State the blood parasite species.
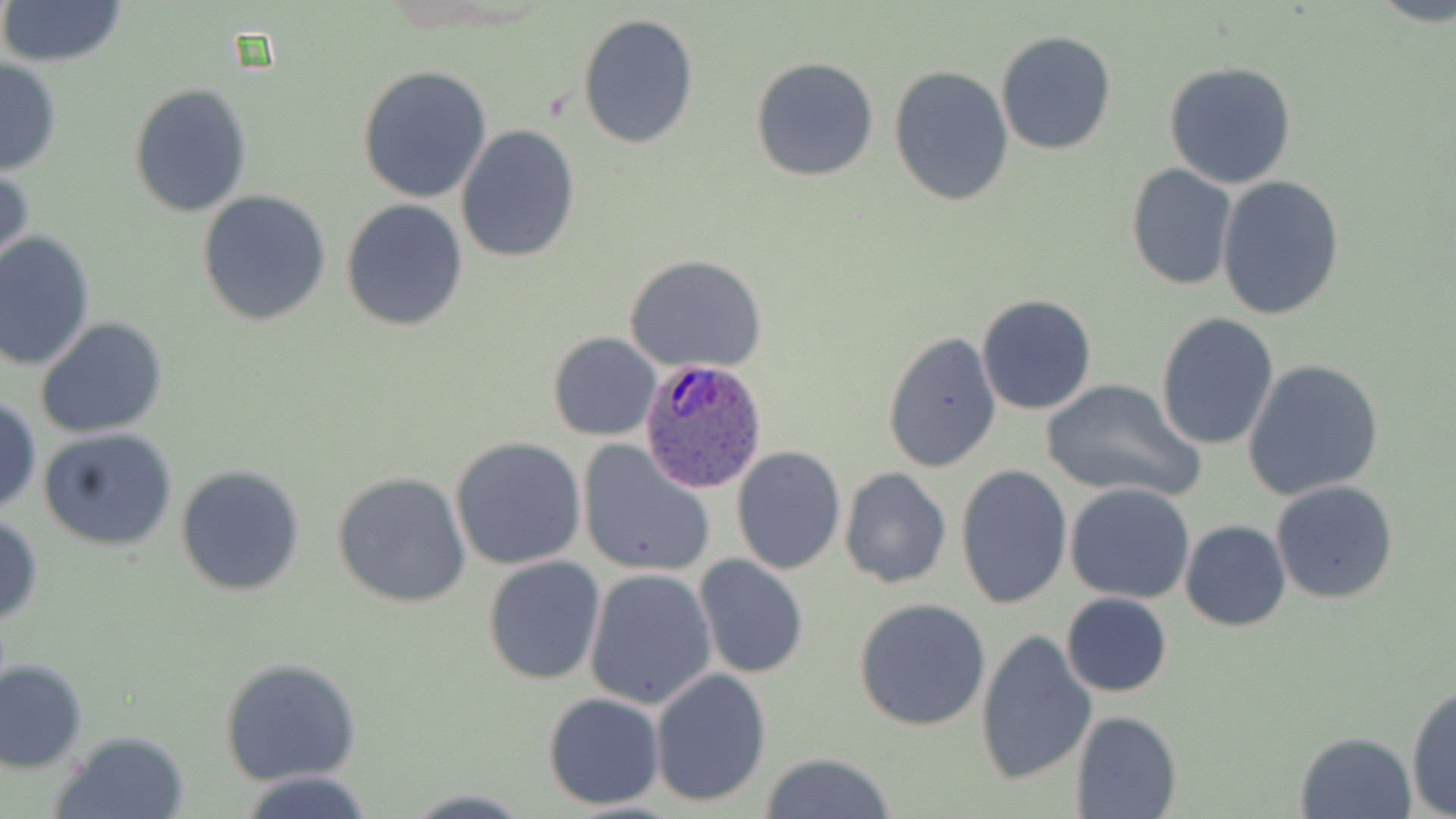

Plasmodium ovale.

Summary:
  - Coordinate format: approximate bounding boxes as [x1, y1, x2, y2] in pixels
  - Plasmodium ovale-infected red blood cell locations: [641, 357, 769, 494]
  - Uninfected red blood cell locations: [0, 0, 131, 68], [577, 14, 699, 149], [996, 30, 1116, 155], [750, 56, 878, 181], [0, 57, 62, 175], [1163, 62, 1297, 189], [357, 65, 492, 204], [889, 66, 1014, 206], [129, 83, 254, 217], [455, 126, 581, 264], [0, 161, 34, 275], [1125, 165, 1236, 288], [1216, 176, 1346, 320], [197, 190, 332, 325], [341, 200, 469, 331], [0, 231, 97, 371], [623, 253, 769, 374], [976, 294, 1097, 415], [1155, 313, 1280, 451], [34, 317, 169, 441], [881, 330, 1002, 472], [548, 333, 660, 442], [1243, 358, 1385, 501], [1040, 379, 1202, 502], [0, 396, 42, 515], [39, 427, 178, 552], [450, 438, 587, 572], [576, 441, 714, 578], [731, 444, 846, 575], [176, 464, 306, 597], [955, 464, 1072, 609], [838, 467, 953, 587], [331, 471, 472, 608], [1270, 480, 1399, 604], [1065, 481, 1196, 603], [0, 513, 44, 626], [1180, 519, 1290, 632], [481, 555, 605, 686], [694, 555, 808, 679], [583, 568, 716, 708], [1059, 592, 1173, 697], [853, 598, 993, 731], [976, 630, 1096, 786], [0, 658, 88, 773], [218, 658, 361, 785], [650, 668, 771, 807], [1407, 683, 1456, 816], [540, 692, 666, 810], [1072, 711, 1182, 819], [52, 730, 191, 818], [1295, 731, 1418, 819], [758, 753, 900, 818], [240, 771, 376, 818]
  - Field of view: one of a larger specimen
  - Preparation: thin blood film
  - Image size: 1456×819 pixels
  - Stain: May-Grünwald-Giemsa
  - Modality: light microscopy
  - Magnification: 1000x